Give the position of every Plasmodium parasite visible.
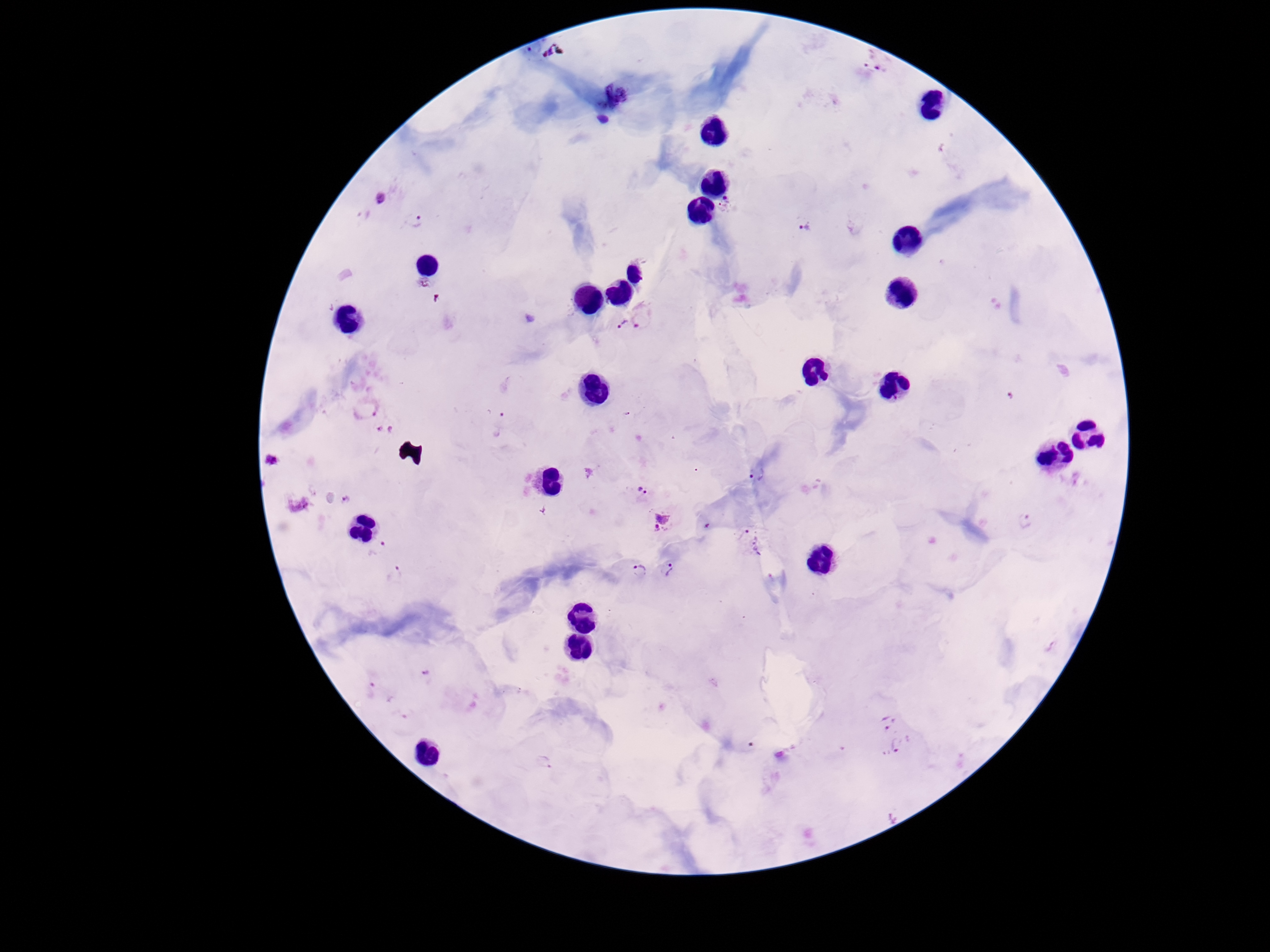
Approximate object centers, in pixels from the top-left corner.
Plasmodium parasites: (x=874, y=63), (x=381, y=199), (x=729, y=207), (x=416, y=222), (x=806, y=228), (x=423, y=284), (x=647, y=314), (x=624, y=324), (x=1011, y=397), (x=366, y=409), (x=501, y=423), (x=273, y=461), (x=757, y=474), (x=640, y=490), (x=346, y=500), (x=661, y=522), (x=1026, y=523), (x=751, y=542), (x=379, y=550), (x=669, y=570), (x=640, y=572), (x=394, y=575), (x=426, y=675), (x=375, y=690), (x=887, y=718), (x=900, y=746), (x=545, y=759).

Summary:
  - Stain: Giemsa
  - Field of view: one from this slide
  - Preparation: thick blood smear
  - Magnification: 100x
  - Capture: smartphone camera through the microscope eyepiece
  - Image size: 1270×952 pixels
  - Patient malaria status: infected